Give the position of every leukocyte visible.
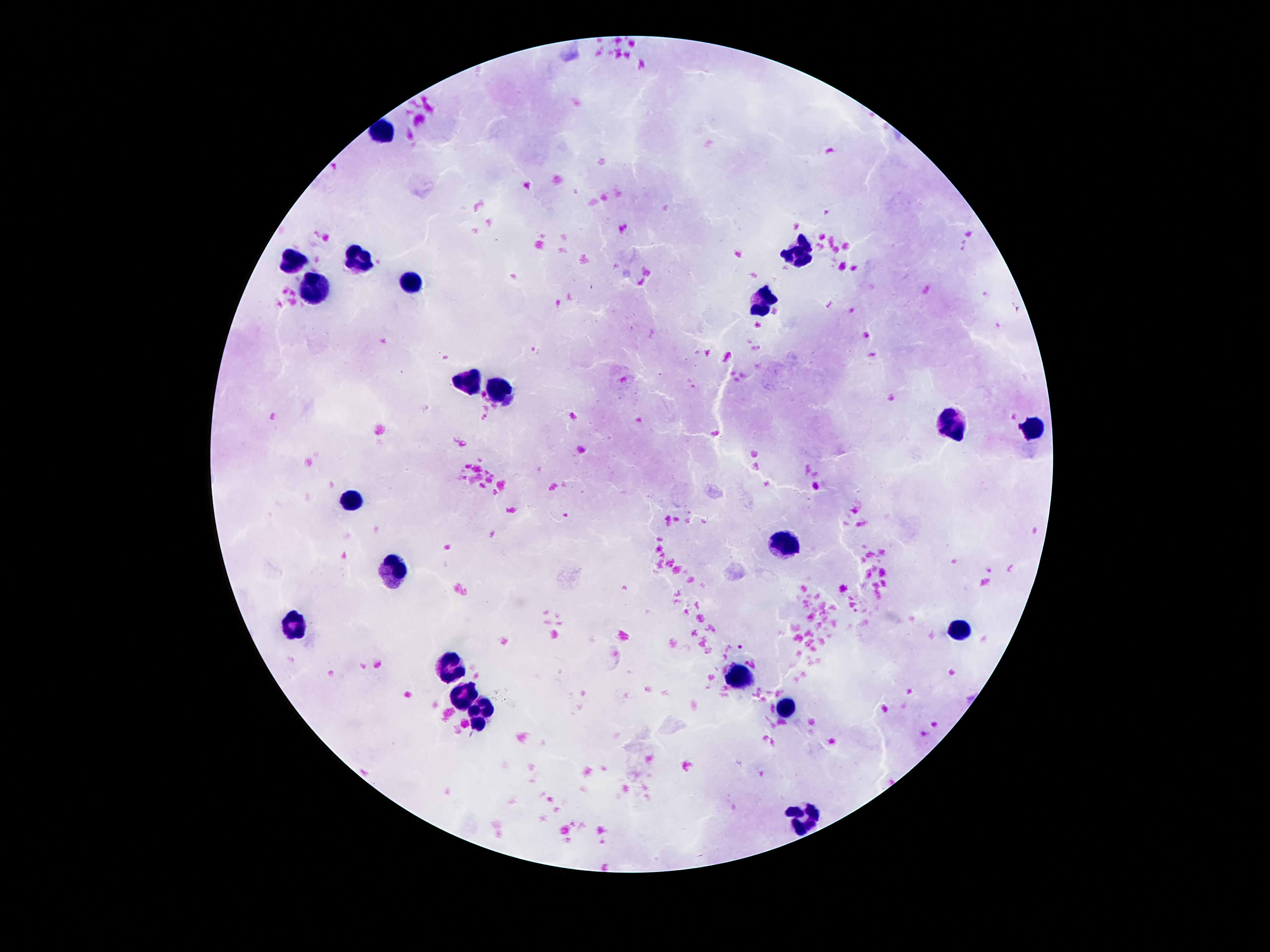
Approximate object centers, in pixels from the top-left corner.
Leukocytes: (x=382, y=128), (x=796, y=253), (x=356, y=260), (x=292, y=262), (x=414, y=281), (x=315, y=290), (x=761, y=301), (x=471, y=386), (x=501, y=387), (x=951, y=426), (x=1035, y=429), (x=352, y=497), (x=787, y=544), (x=389, y=568), (x=296, y=620), (x=958, y=629), (x=451, y=670), (x=742, y=679), (x=464, y=696), (x=787, y=712), (x=481, y=717), (x=805, y=816).

stain = Giemsa
preparation = thick peripheral-blood smear
magnification = 100x
image size = 1270×952 pixels
patient malaria status = uninfected
capture = smartphone camera through the microscope eyepiece
field of view = one from this slide